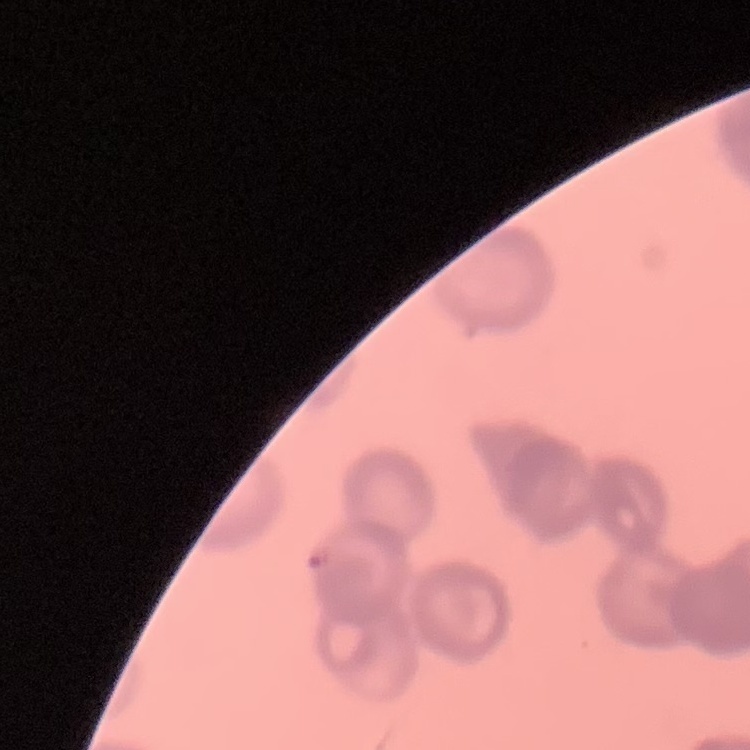

The erythrocytes exhibit rouleaux formation. Square crop of a larger photomicrograph. Field's or Giemsa stain. Thin blood smear.